Comment on the morphology of the erythrocytes.
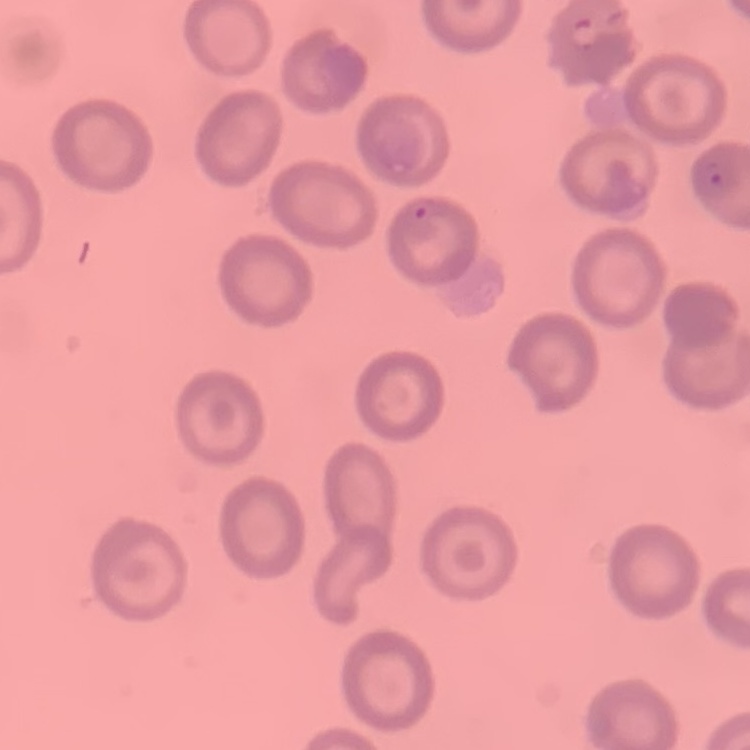
No rouleaux formation.

Summary:
  - Stain: Field's or Giemsa
  - Preparation: thin blood film
  - Image type: square crop of a larger photomicrograph